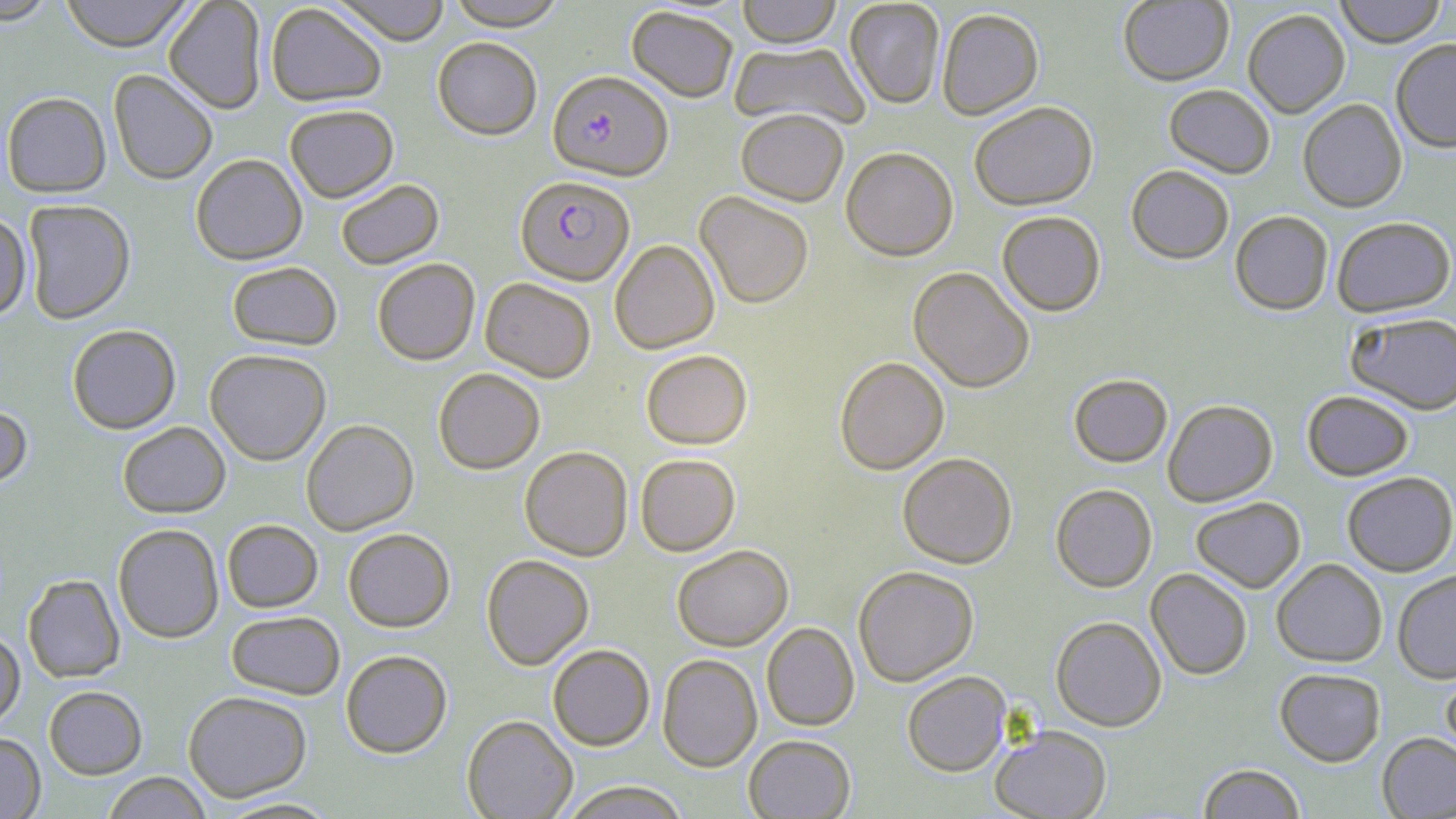
Approximate bounding boxes as (x1, y1, x2, y2) in pixels. Plasmodium falciparum-infected red blood cell locations: (548, 70, 673, 180), (515, 175, 635, 285). Uninfected red blood cell locations: (0, 0, 60, 25), (60, 0, 193, 52), (164, 0, 267, 114), (331, 0, 452, 45), (737, 0, 842, 48), (845, 0, 945, 109), (1333, 0, 1448, 47), (445, 1, 568, 31), (1118, 1, 1234, 86), (265, 3, 388, 106), (626, 6, 738, 102), (936, 8, 1044, 120), (1242, 9, 1350, 118), (432, 37, 542, 139), (1391, 38, 1456, 153), (729, 41, 870, 131), (108, 69, 218, 185), (1163, 84, 1275, 179), (1, 91, 111, 197), (1297, 99, 1407, 212), (969, 101, 1098, 210), (284, 104, 399, 202), (736, 108, 848, 206), (841, 146, 958, 261), (190, 153, 307, 265), (1127, 165, 1234, 264), (335, 178, 444, 269), (696, 190, 813, 309), (22, 199, 136, 324), (997, 211, 1105, 316), (1230, 211, 1333, 315), (0, 212, 31, 320), (1331, 216, 1455, 316), (609, 239, 720, 354), (372, 258, 480, 365), (227, 261, 342, 350), (908, 266, 1034, 393), (480, 277, 596, 382), (1345, 312, 1456, 415), (67, 324, 181, 434), (204, 348, 331, 465), (641, 349, 752, 449), (834, 356, 949, 475), (433, 368, 545, 474), (1069, 374, 1173, 468), (1302, 390, 1414, 480), (1163, 399, 1278, 506), (0, 404, 33, 489), (301, 419, 419, 535), (118, 421, 230, 518), (519, 446, 633, 561), (897, 453, 1017, 568), (635, 454, 740, 556), (1342, 471, 1456, 576), (1051, 484, 1157, 592), (1190, 497, 1306, 593), (222, 519, 323, 613), (113, 523, 224, 643), (343, 528, 455, 632), (672, 544, 793, 651), (481, 554, 594, 669), (1272, 558, 1387, 667), (853, 565, 979, 686), (1146, 568, 1253, 680), (1392, 569, 1456, 683), (22, 574, 125, 683), (226, 610, 345, 699), (1050, 615, 1167, 730), (761, 622, 859, 731), (0, 629, 25, 729), (548, 644, 655, 750), (341, 650, 452, 758), (658, 654, 762, 772), (1440, 665, 1456, 766), (1275, 667, 1386, 766), (902, 671, 1011, 776), (43, 685, 148, 779), (183, 690, 312, 802), (462, 715, 578, 819), (990, 725, 1112, 819), (0, 732, 45, 819), (1377, 732, 1456, 818), (743, 734, 856, 818), (1198, 763, 1306, 819), (101, 772, 213, 818), (560, 781, 690, 819), (216, 797, 342, 818). Slide-level diagnosis: Plasmodium falciparum. Captured at 1000x magnification. Thin blood smear. May-Grünwald-Giemsa-stained preparation. Single field of view. Optical microscopy. Image is 1456×819 pixels.